Comment on the morphology of the red blood cells.
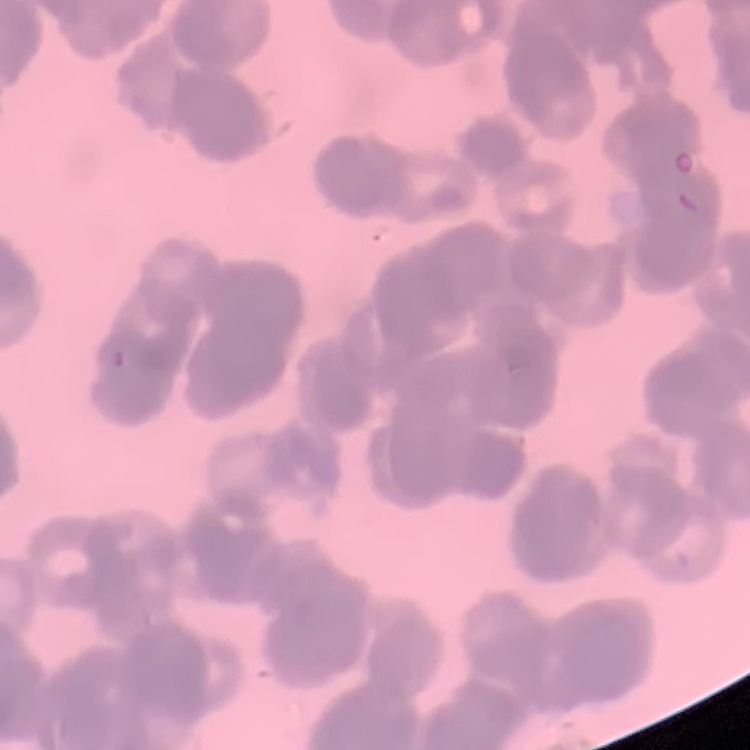
They show rouleaux formation.

Square crop of a larger photomicrograph. Field's or Giemsa stain. Thin blood smear.